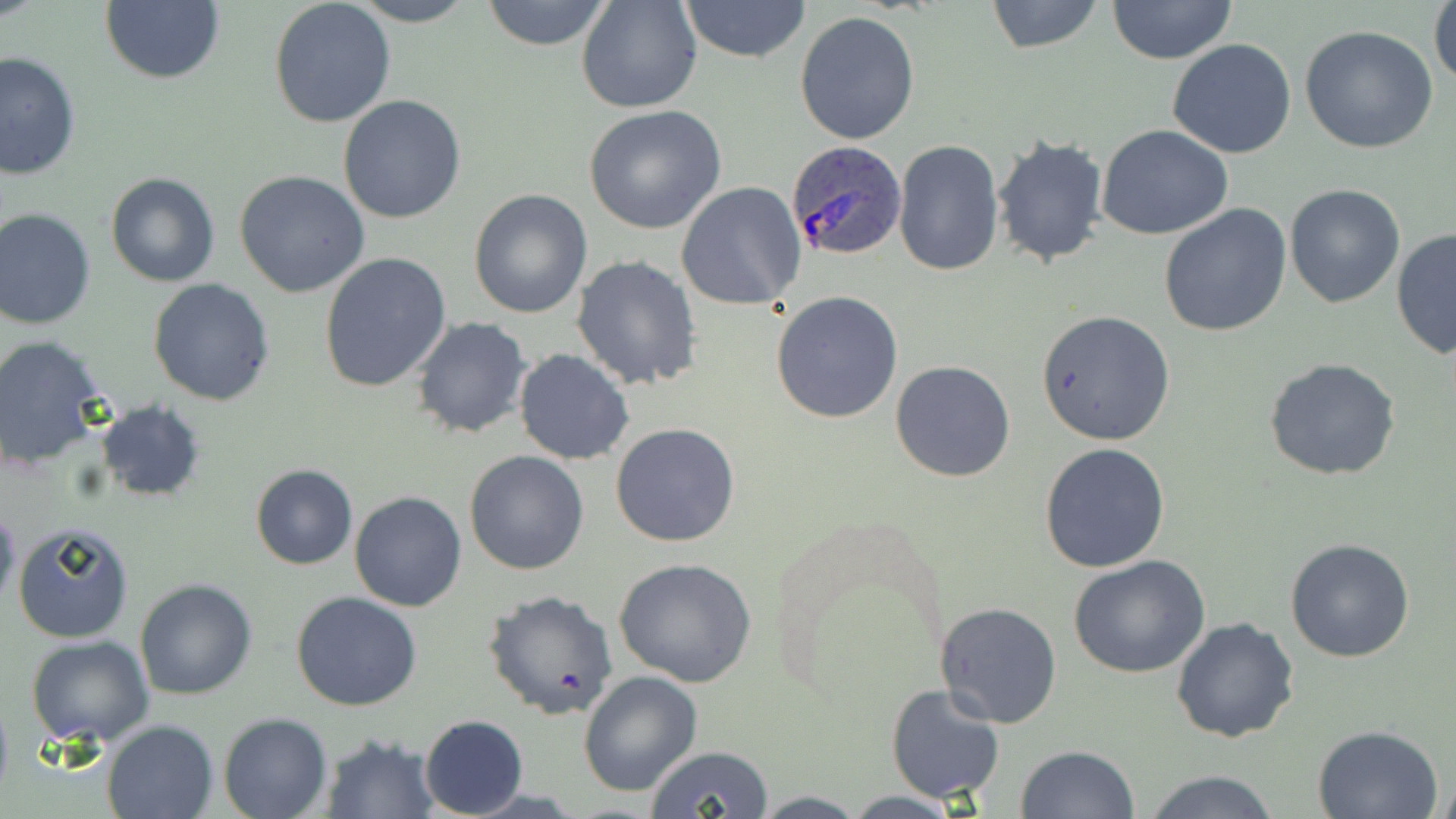
Approximate bounding boxes as [x1, y1, x2, y2] in pixels. Plasmodium ovale-infected red blood cell locations: [785, 141, 907, 261]. Uninfected red blood cell locations: [351, 0, 480, 26], [480, 0, 612, 50], [576, 0, 702, 113], [679, 0, 810, 62], [984, 0, 1107, 53], [1106, 0, 1238, 65], [1430, 0, 1456, 91], [99, 2, 225, 85], [269, 3, 397, 128], [795, 11, 920, 145], [1300, 25, 1438, 154], [1167, 38, 1297, 157], [0, 51, 80, 182], [338, 95, 468, 224], [583, 105, 727, 233], [1097, 125, 1235, 241], [992, 136, 1109, 267], [893, 139, 1005, 279], [234, 169, 370, 297], [105, 172, 220, 287], [676, 182, 805, 311], [1284, 184, 1405, 308], [469, 187, 594, 319], [1158, 204, 1291, 337], [0, 208, 96, 330], [1391, 229, 1455, 360], [318, 253, 453, 395], [573, 255, 702, 392], [149, 279, 275, 405], [770, 291, 904, 424], [1036, 311, 1176, 445], [411, 317, 532, 439], [0, 335, 111, 471], [514, 348, 634, 464], [1264, 358, 1404, 481], [890, 359, 1017, 482], [95, 399, 207, 504], [611, 422, 741, 547], [1040, 442, 1170, 573], [464, 450, 590, 575], [250, 464, 358, 569], [350, 490, 468, 611], [0, 499, 20, 614], [12, 520, 134, 644], [1285, 536, 1416, 662], [1069, 556, 1210, 679], [614, 558, 758, 688], [135, 577, 257, 700], [484, 589, 618, 718], [291, 592, 423, 711], [936, 602, 1062, 728], [1170, 616, 1298, 742], [26, 636, 155, 749], [577, 670, 703, 796], [885, 683, 1006, 804], [0, 689, 12, 806], [218, 713, 333, 819], [419, 715, 526, 818], [101, 719, 217, 819], [1312, 723, 1444, 818], [321, 731, 439, 817], [1016, 745, 1139, 819], [645, 746, 774, 818], [1140, 771, 1282, 819]. Slide-level diagnosis: Plasmodium ovale. Thin blood film. One field of a larger specimen. Image is 1456×819 pixels. May-Grünwald-Giemsa stain. Optical microscopy. Captured at 1000x magnification.